Outline platelets.
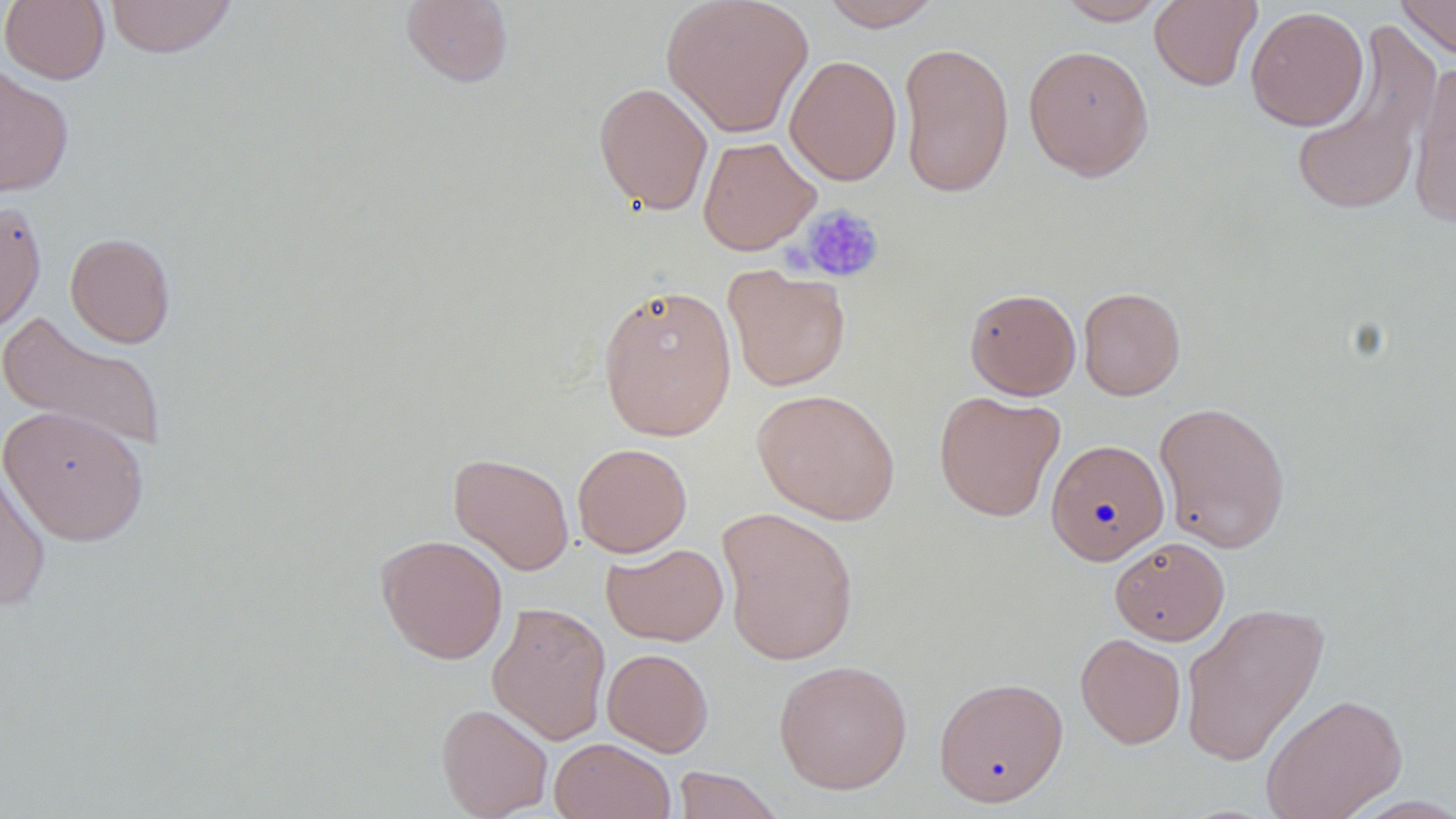

Approximate bounding boxes as [x1, y1, x2, y2] in pixels.
Platelets: [798, 205, 884, 284].

slide-level diagnosis = no evidence of blood parasites
preparation = thin blood smear
field of view = one of a larger specimen
modality = optical microscopy
image size = 1456×819 pixels
magnification = 1000x
stain = May-Grünwald-Giemsa
uninfected red blood cell locations = approximate bounding boxes as [x1, y1, x2, y2] in pixels: [1, 0, 110, 84], [104, 0, 238, 58], [401, 0, 514, 88], [660, 0, 815, 137], [818, 0, 942, 30], [1056, 0, 1168, 25], [1148, 0, 1262, 91], [1395, 0, 1456, 62], [1245, 5, 1369, 131], [1289, 28, 1441, 219], [898, 41, 1015, 199], [1023, 44, 1154, 181], [784, 54, 902, 185], [1409, 60, 1456, 229], [0, 64, 75, 198], [593, 81, 713, 216], [698, 136, 820, 255], [0, 198, 47, 338], [65, 232, 176, 348], [723, 264, 851, 391], [597, 283, 738, 441], [1078, 286, 1186, 400], [965, 288, 1081, 400], [1, 311, 169, 455], [751, 388, 900, 525], [934, 390, 1066, 522], [1153, 400, 1291, 553], [1, 404, 149, 546], [1045, 438, 1169, 566], [572, 442, 692, 557], [448, 452, 575, 575], [0, 465, 51, 611], [716, 507, 860, 666], [375, 533, 509, 664], [1109, 537, 1230, 645], [601, 543, 729, 646], [487, 602, 612, 744], [1180, 602, 1329, 767], [1075, 633, 1187, 749], [602, 648, 713, 756], [773, 659, 912, 794], [933, 676, 1068, 806], [1261, 693, 1408, 819], [436, 702, 553, 819], [548, 737, 676, 819], [670, 767, 784, 818]